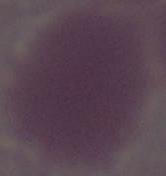

Summary:
  - Identification: erythrocyte
  - Magnification: 1000x
  - Modality: micrograph